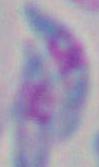 Toxoplasma gondii is seen. Micrograph. 1000x magnification.